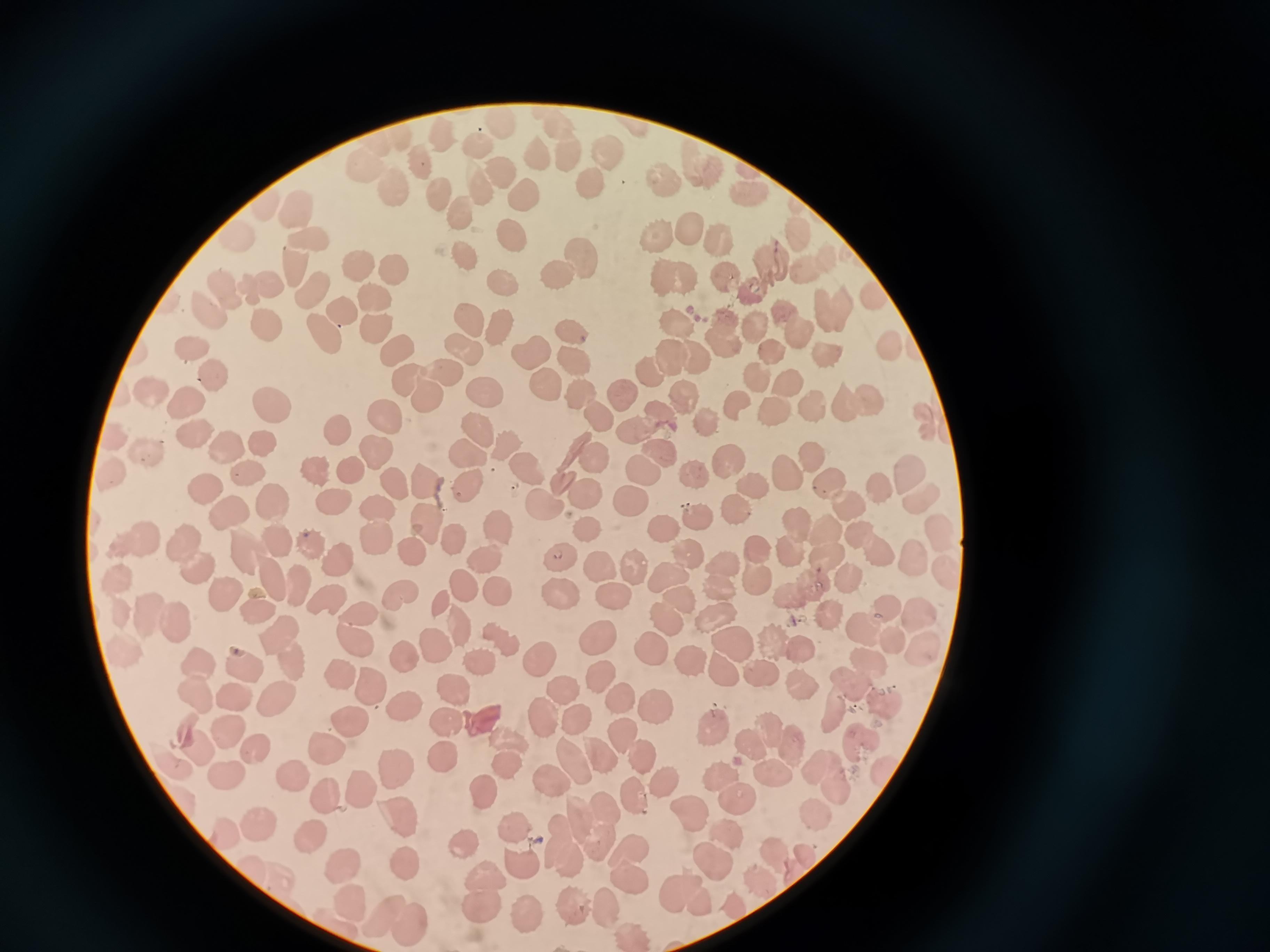

Approximate centers as {x, y} in pixels. Cell locations: {442, 140}, {476, 144}, {613, 148}, {536, 153}, {574, 155}, {422, 164}, {698, 166}, {362, 167}, {500, 172}, {596, 180}, {667, 180}, {391, 192}, {527, 193}, {437, 194}, {297, 211}, {460, 212}, {687, 228}, {654, 234}, {510, 235}, {312, 239}, {719, 241}, {465, 254}, {570, 264}, {297, 269}, {357, 269}, {392, 270}, {815, 270}, {764, 275}, {673, 277}, {725, 278}, {504, 284}, {261, 288}, {317, 291}, {229, 293}, {376, 302}, {213, 310}, {831, 311}, {343, 314}, {470, 317}, {674, 321}, {791, 326}, {267, 327}, {498, 327}, {377, 328}, {754, 328}, {324, 333}, {725, 333}, {574, 335}, {468, 346}, {892, 346}, {192, 349}, {773, 351}, {396, 353}, {528, 355}, {836, 356}, {673, 362}, {572, 363}, {212, 376}, {756, 379}, {785, 380}, {551, 386}, {425, 387}, {481, 390}, {622, 393}, {151, 394}, {582, 394}, {684, 396}, {856, 402}, {272, 405}, {186, 406}, {737, 406}, {811, 409}, {773, 410}, {385, 419}, {596, 420}, {705, 423}, {644, 428}, {337, 430}, {476, 432}, {196, 433}, {266, 443}, {507, 445}, {230, 448}, {147, 451}, {812, 451}, {665, 452}, {468, 454}, {376, 455}, {597, 458}, {727, 461}, {910, 467}, {528, 468}, {788, 469}, {314, 470}, {645, 472}, {110, 473}, {251, 473}, {352, 473}, {694, 476}, {425, 481}, {395, 483}, {876, 485}, {471, 486}, {757, 486}, {206, 488}, {836, 491}, {582, 495}, {270, 501}, {339, 502}, {632, 502}, {546, 503}, {739, 512}, {228, 513}, {696, 515}, {429, 526}, {588, 527}, {380, 528}, {499, 528}, {665, 528}, {796, 540}, {829, 542}, {454, 544}, {870, 544}, {132, 545}, {308, 545}, {684, 549}, {412, 554}, {186, 556}, {341, 556}, {559, 557}, {260, 560}, {486, 560}, {636, 568}, {757, 568}, {602, 572}, {718, 572}, {669, 576}, {854, 579}, {298, 585}, {462, 585}, {806, 589}, {500, 592}, {221, 593}, {615, 594}, {327, 596}, {559, 596}, {402, 599}, {676, 601}, {441, 605}, {257, 606}, {884, 610}, {712, 614}, {829, 616}, {163, 621}, {667, 622}, {459, 626}, {361, 628}, {863, 629}, {600, 635}, {501, 637}, {439, 642}, {788, 642}, {731, 643}, {282, 647}, {652, 651}, {538, 657}, {406, 660}, {692, 660}, {244, 662}, {483, 662}, {722, 672}, {341, 673}, {761, 676}, {864, 676}, {601, 677}, {197, 684}, {376, 684}, {806, 684}, {453, 687}, {563, 689}, {276, 697}, {622, 699}, {886, 704}, {403, 707}, {660, 707}, {833, 712}, {545, 721}, {351, 722}, {576, 722}, {449, 723}, {480, 723}, {718, 728}, {227, 730}, {623, 736}, {862, 738}, {773, 739}, {193, 740}, {328, 746}, {252, 751}, {512, 754}, {607, 754}, {440, 759}, {640, 759}, {577, 762}, {395, 767}, {770, 770}, {224, 775}, {294, 775}, {832, 777}, {550, 778}, {666, 781}, {728, 787}, {358, 788}, {486, 790}, {322, 794}, {635, 801}, {690, 809}, {813, 810}, {402, 814}, {590, 824}, {258, 826}, {514, 826}, {732, 832}, {313, 834}, {568, 846}, {464, 848}, {403, 859}, {716, 860}, {520, 861}, {345, 865}, {637, 869}, {484, 895}, {687, 895}, {352, 903}, {570, 907}, {608, 908}, {520, 914}, {399, 921}. Single field of view. Image is 1270×952 pixels. Giemsa-stained preparation. Thin smear of blood. Photographed with a smartphone camera at the microscope eyepiece.